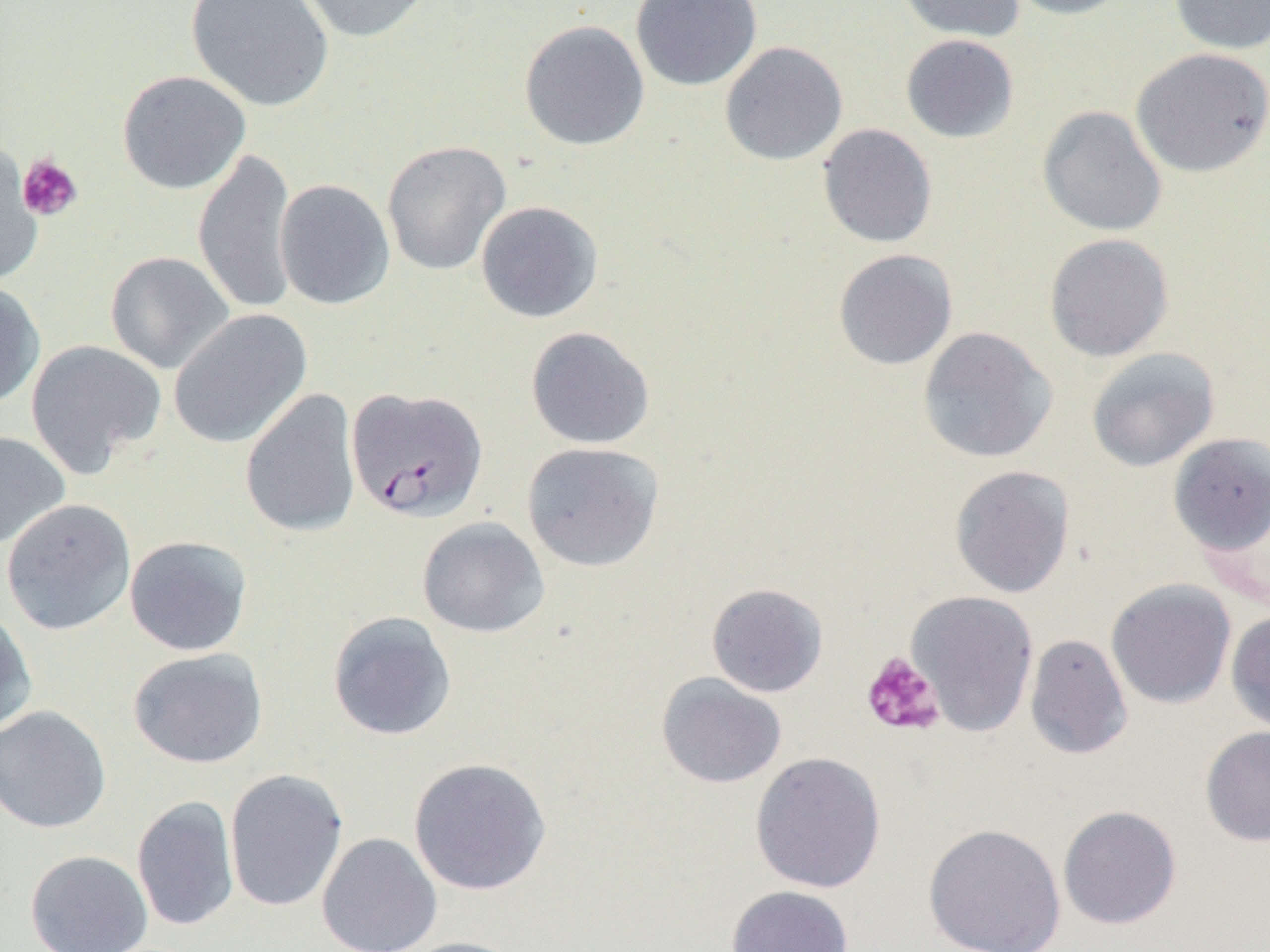

Approximate bounding boxes as named x1/y1/x2/y2 corners in pixels. Platelet locations: (x1=16, y1=153, x2=83, y2=222), (x1=861, y1=651, x2=945, y2=737). Plasmodium falciparum-infected red blood cell locations: (x1=347, y1=387, x2=488, y2=523). Uninfected red blood cell locations: (x1=184, y1=0, x2=335, y2=112), (x1=290, y1=0, x2=436, y2=44), (x1=630, y1=0, x2=762, y2=91), (x1=894, y1=0, x2=1026, y2=43), (x1=1005, y1=0, x2=1135, y2=20), (x1=1168, y1=0, x2=1270, y2=55), (x1=519, y1=20, x2=650, y2=151), (x1=900, y1=34, x2=1019, y2=143), (x1=719, y1=41, x2=848, y2=166), (x1=1130, y1=47, x2=1270, y2=178), (x1=117, y1=70, x2=251, y2=195), (x1=1037, y1=105, x2=1168, y2=237), (x1=817, y1=123, x2=938, y2=248), (x1=382, y1=140, x2=511, y2=276), (x1=0, y1=142, x2=43, y2=285), (x1=193, y1=146, x2=299, y2=316), (x1=274, y1=179, x2=395, y2=310), (x1=475, y1=201, x2=604, y2=323), (x1=1044, y1=233, x2=1174, y2=362), (x1=833, y1=248, x2=958, y2=370), (x1=104, y1=251, x2=235, y2=374), (x1=0, y1=280, x2=45, y2=409), (x1=168, y1=309, x2=312, y2=449), (x1=525, y1=326, x2=655, y2=450), (x1=917, y1=326, x2=1057, y2=463), (x1=25, y1=339, x2=167, y2=478), (x1=1086, y1=347, x2=1220, y2=472), (x1=240, y1=388, x2=361, y2=539), (x1=0, y1=430, x2=71, y2=549), (x1=1167, y1=433, x2=1270, y2=557), (x1=521, y1=441, x2=664, y2=572), (x1=949, y1=464, x2=1075, y2=598), (x1=1, y1=498, x2=136, y2=636), (x1=417, y1=516, x2=549, y2=638), (x1=124, y1=535, x2=253, y2=657), (x1=1106, y1=579, x2=1236, y2=709), (x1=706, y1=583, x2=828, y2=697), (x1=906, y1=590, x2=1039, y2=736), (x1=0, y1=607, x2=37, y2=736), (x1=1226, y1=610, x2=1270, y2=733), (x1=328, y1=611, x2=458, y2=741), (x1=1024, y1=633, x2=1133, y2=760), (x1=128, y1=647, x2=268, y2=769), (x1=656, y1=673, x2=787, y2=789), (x1=0, y1=705, x2=111, y2=834), (x1=1200, y1=725, x2=1270, y2=847), (x1=750, y1=751, x2=887, y2=894), (x1=408, y1=757, x2=552, y2=895), (x1=225, y1=769, x2=348, y2=912), (x1=132, y1=795, x2=240, y2=932), (x1=1057, y1=805, x2=1182, y2=930), (x1=923, y1=822, x2=1067, y2=952), (x1=317, y1=833, x2=442, y2=952), (x1=25, y1=850, x2=153, y2=952), (x1=725, y1=885, x2=854, y2=952), (x1=394, y1=936, x2=527, y2=952). Slide-level diagnosis: Plasmodium falciparum. Image is 1270×952 pixels. Optical microscopy. Single field of view. Thin blood film. 1000x magnification.